Name the blood parasite species.
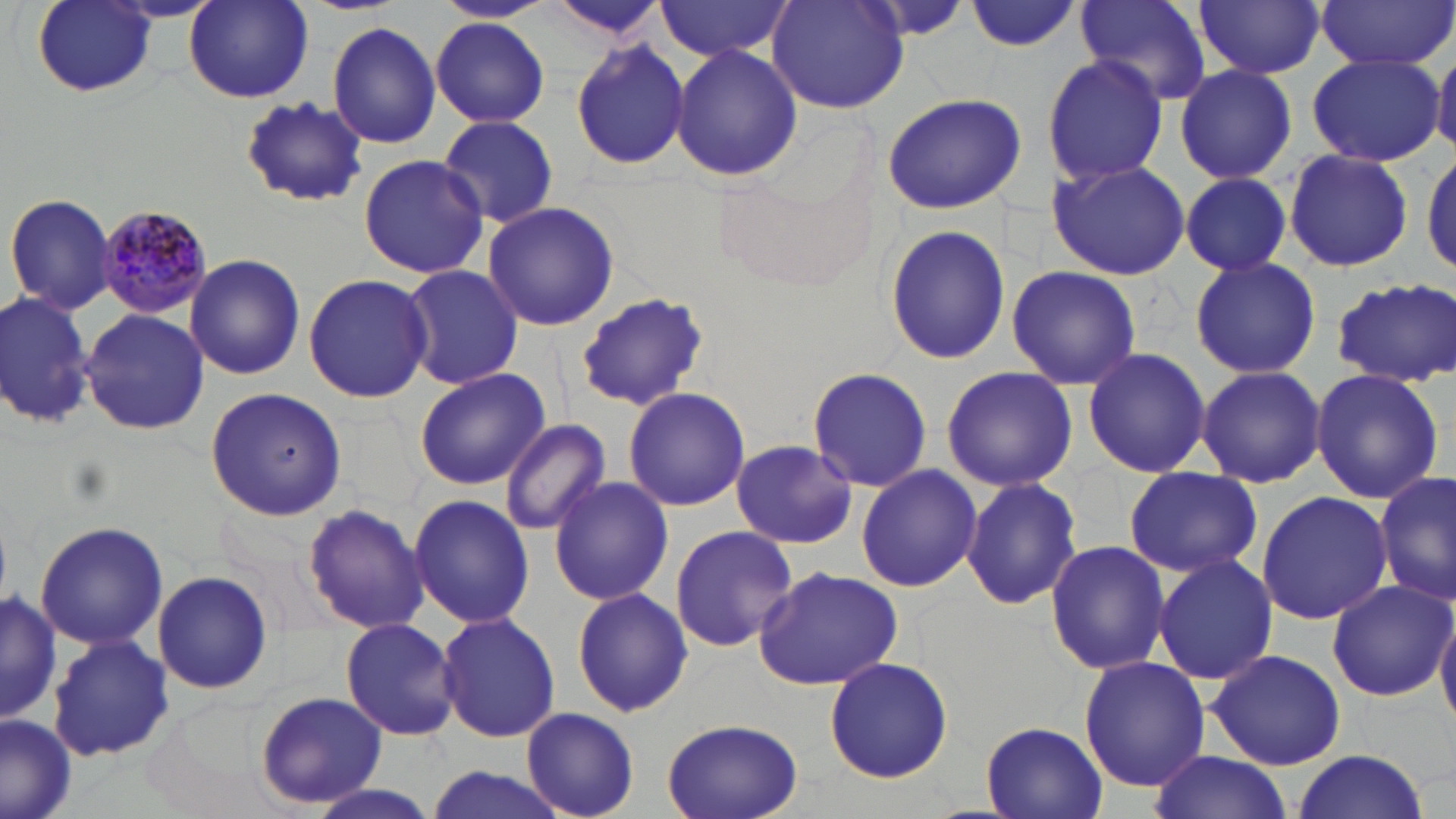

Plasmodium malariae.

Summary:
  - Coordinate format: approximate bounding boxes as [x1, y1, x2, y2] in pixels
  - Uninfected red blood cell locations: [32, 0, 158, 98], [182, 0, 315, 105], [1074, 0, 1212, 106], [1195, 0, 1324, 79], [1318, 0, 1454, 70], [544, 1, 671, 42], [654, 1, 796, 61], [768, 1, 911, 115], [966, 1, 1084, 52], [431, 17, 550, 128], [327, 22, 442, 150], [570, 40, 692, 172], [671, 45, 804, 180], [1307, 51, 1444, 167], [1433, 52, 1456, 156], [1041, 54, 1169, 187], [1173, 64, 1298, 186], [881, 94, 1026, 214], [238, 97, 369, 207], [436, 113, 561, 229], [1422, 147, 1456, 276], [1284, 148, 1413, 273], [357, 153, 488, 281], [1046, 160, 1191, 280], [1176, 173, 1296, 276], [4, 192, 118, 315], [482, 201, 620, 331], [884, 225, 1010, 366], [186, 253, 305, 379], [1189, 254, 1320, 380], [401, 264, 523, 391], [1005, 265, 1141, 391], [303, 272, 433, 404], [1331, 278, 1456, 386], [0, 288, 97, 430], [574, 292, 710, 410], [80, 309, 210, 435], [1083, 348, 1210, 478], [1196, 364, 1325, 489], [806, 366, 932, 493], [414, 367, 549, 492], [941, 367, 1076, 492], [1309, 369, 1444, 504], [623, 386, 750, 513], [205, 388, 346, 521], [500, 418, 612, 536], [730, 444, 858, 547], [855, 463, 983, 593], [1123, 468, 1263, 579], [1376, 470, 1454, 609], [548, 476, 673, 607], [961, 476, 1083, 612], [1257, 490, 1392, 624], [409, 495, 533, 627], [301, 502, 431, 634], [34, 521, 168, 651], [668, 523, 801, 654], [1044, 539, 1171, 675], [1150, 552, 1281, 687], [753, 564, 903, 690], [152, 568, 273, 697], [1326, 578, 1454, 701], [0, 588, 62, 722], [571, 588, 693, 718], [1437, 605, 1456, 731], [436, 612, 560, 742], [339, 617, 460, 741], [46, 635, 175, 762], [1206, 649, 1348, 771], [1078, 655, 1209, 794], [824, 657, 953, 783], [255, 691, 387, 811], [522, 706, 638, 818], [0, 713, 80, 819], [659, 718, 805, 819], [980, 722, 1107, 818], [1291, 750, 1428, 817], [1147, 751, 1293, 819], [421, 766, 571, 819], [302, 784, 443, 819]
  - Plasmodium malariae-infected red blood cell locations: [99, 204, 213, 317]
  - Image size: 1456×819 pixels
  - Field of view: single
  - Stain: May-Grünwald-Giemsa
  - Modality: optical microscopy
  - Magnification: 1000x
  - Preparation: thin blood film